Report the malaria status of this cell.
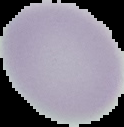

It is uninfected.

image_type: segmented cell region on a black background
preparation: thin blood smear
image_size: 124×127 pixels